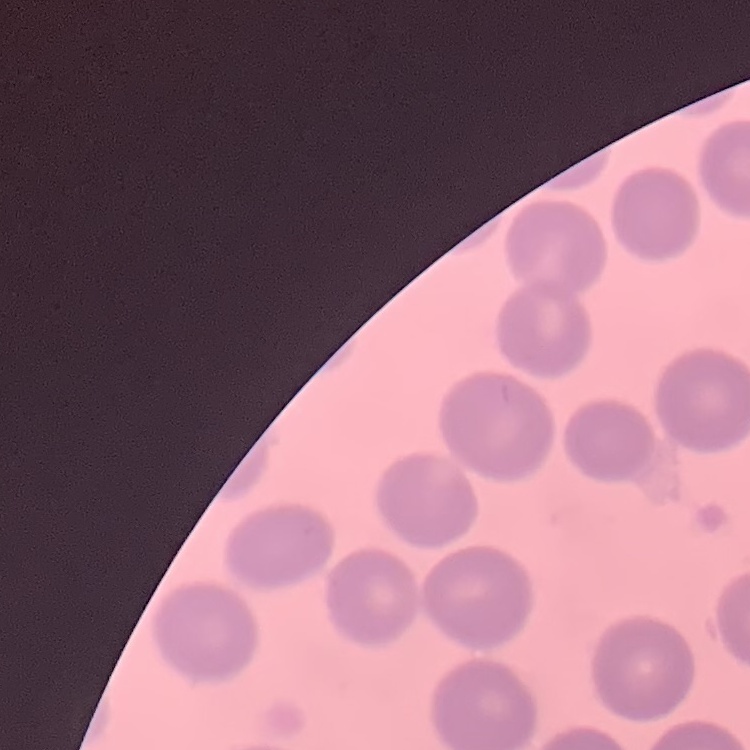
The erythrocytes exhibit no rouleaux formation. Square crop of a larger photomicrograph. Thin peripheral smear. Stained with either Field's or Giemsa.